State which cell type is depicted.
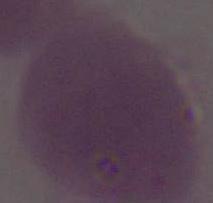

An erythrocyte.

Summary:
  - Modality: photomicrograph
  - Magnification: 1000x